Give the position of every malaria parasite.
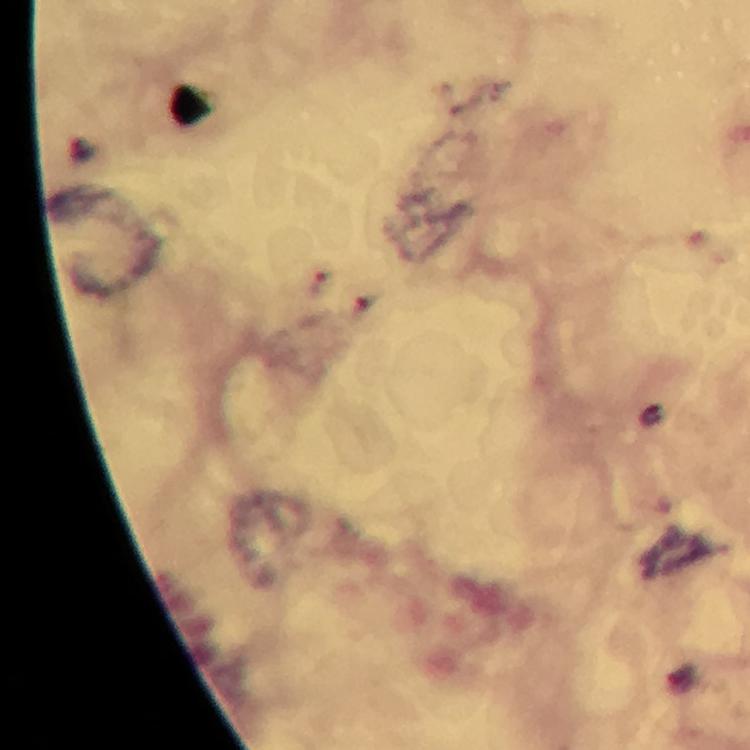

Approximate centers as [x, y] in pixels.
Malaria parasites: [321, 283].

100x magnification. Photographed through the microscope with a smartphone camera. A crop from one field of view. Immersion oil was used. Giemsa-stained preparation. From a malaria diagnostic workup. Thick smear. Image is 750×750 pixels.